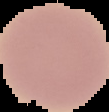
preparation = thin blood smear
image type = segmented cell region on a black background
image size = 109×112 pixels
malaria status = uninfected